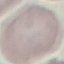
Malaria status: uninfected. Giemsa stain. Acquired by smartphone through the microscope eyepiece. Automatically extracted cell patch, resized to 64 × 64 pixels. Thin blood film.